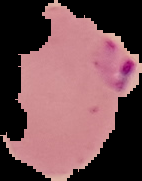
The area outside the segmented cell region is set to black. Image is 142×181 pixels. Malaria status: parasitized. From a thin blood film.